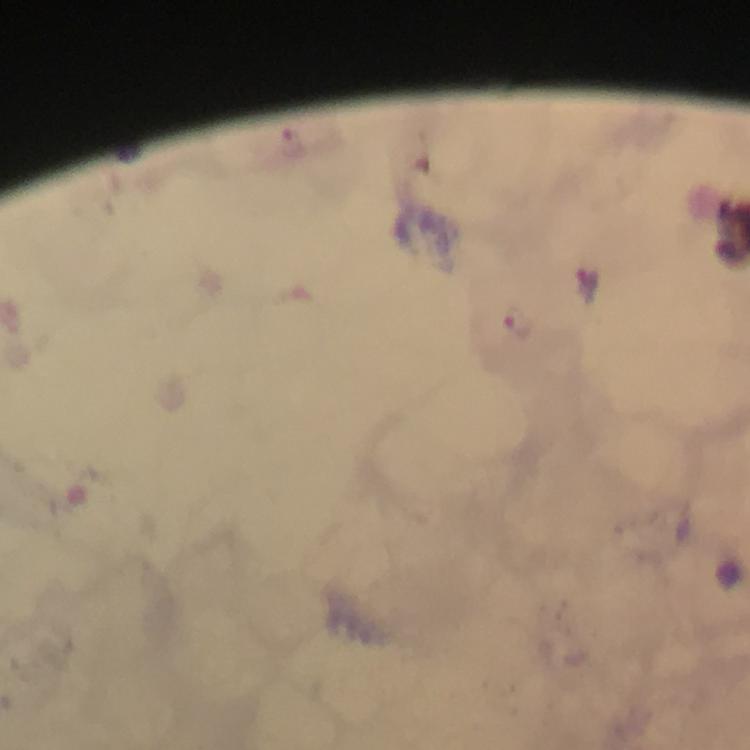
Approximate object centers, in pixels from the top-left corner.
Summary:
  - Plasmodium parasite locations: (x=587, y=284), (x=518, y=322)
  - Magnification: 100x
  - Preparation: thick blood film
  - Immersion oil: used
  - Image size: 750×750 pixels
  - Stain: Giemsa
  - Cropped from: a single field of view
  - Capture: smartphone photograph through a microscope
  - Context: from a malaria diagnostic workup